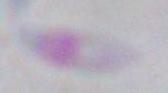

identification = Toxoplasma gondii
modality = micrograph
magnification = 1000x